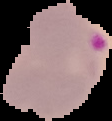

Summary:
  - Preparation: thin blood smear
  - Image size: 112×121 pixels
  - Image type: cell region segmented out of the field of view; surrounding area masked to black
  - Result: malaria parasites identified